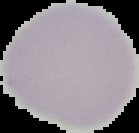

The area outside the segmented cell region is set to black. From a thin blood film. Image is 139×133 pixels. Result: no Plasmodium parasites detected.